Give the preparation type.
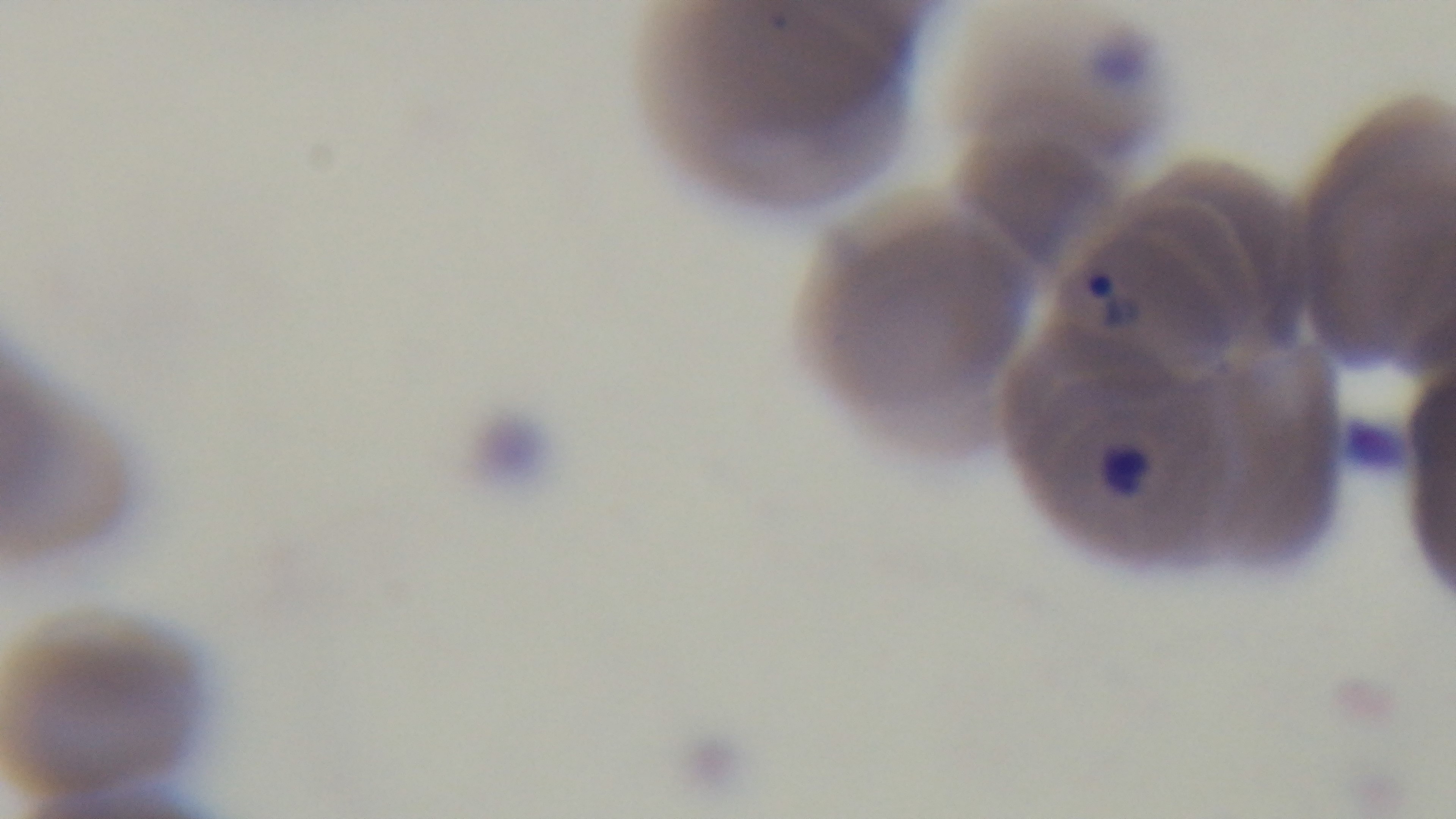

A thin smear.

modality = light microscopy
field of view = single
stain = Giemsa
malaria status = positive
capture = mounted 4K digital camera
objective = 100x oil immersion